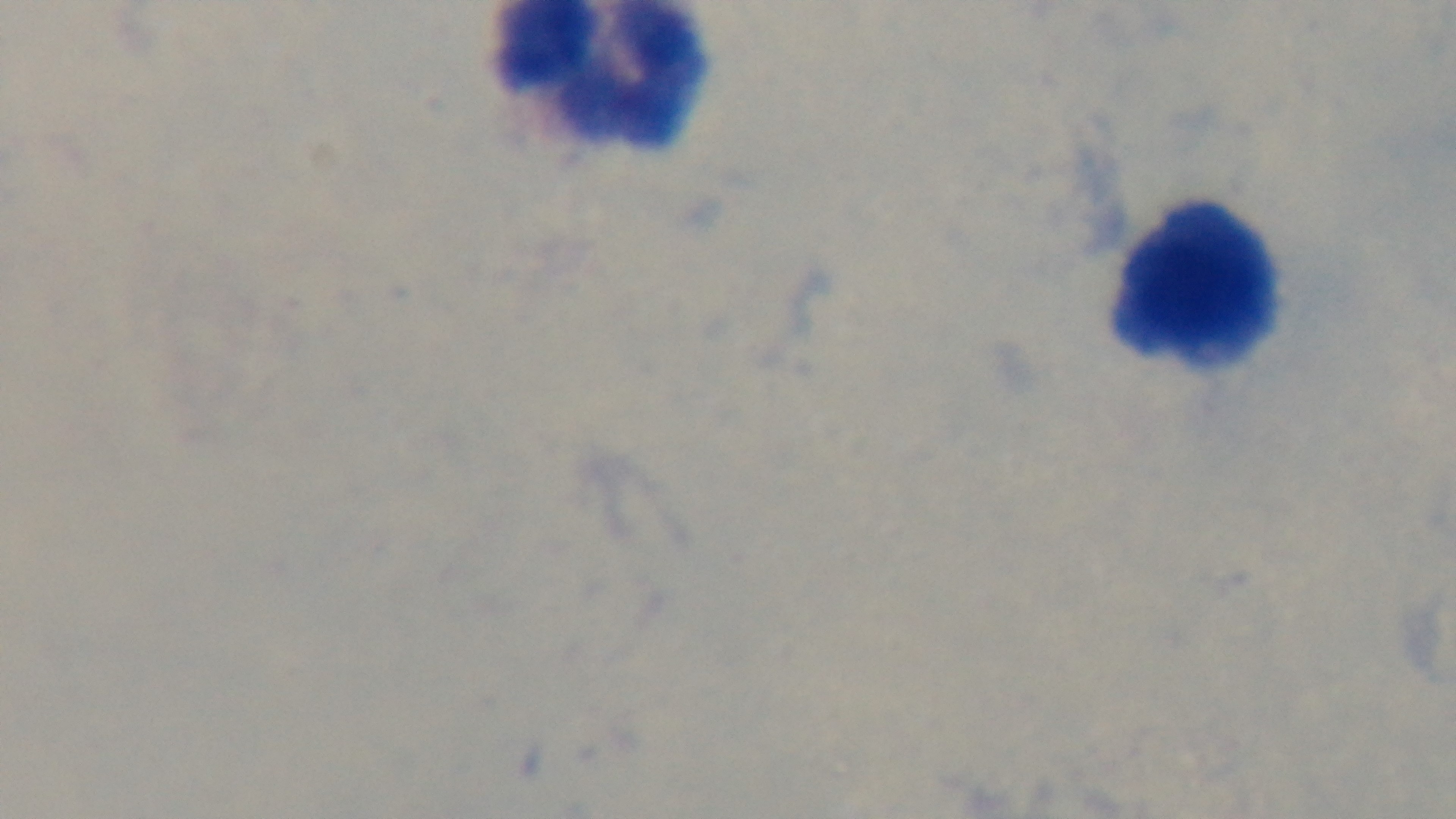

Summary:
  - Capture: mounted 4K digital camera
  - Objective: 100x oil immersion
  - Preparation: thick
  - Stain: Giemsa
  - Modality: light microscopy
  - Malaria status: negative
  - Field of view: single